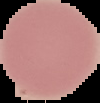

Summary:
  - Image size: 100×103 pixels
  - Preparation: thin blood film
  - Result: no malaria parasites detected
  - Image type: cell region segmented out of the field of view; surrounding area masked to black